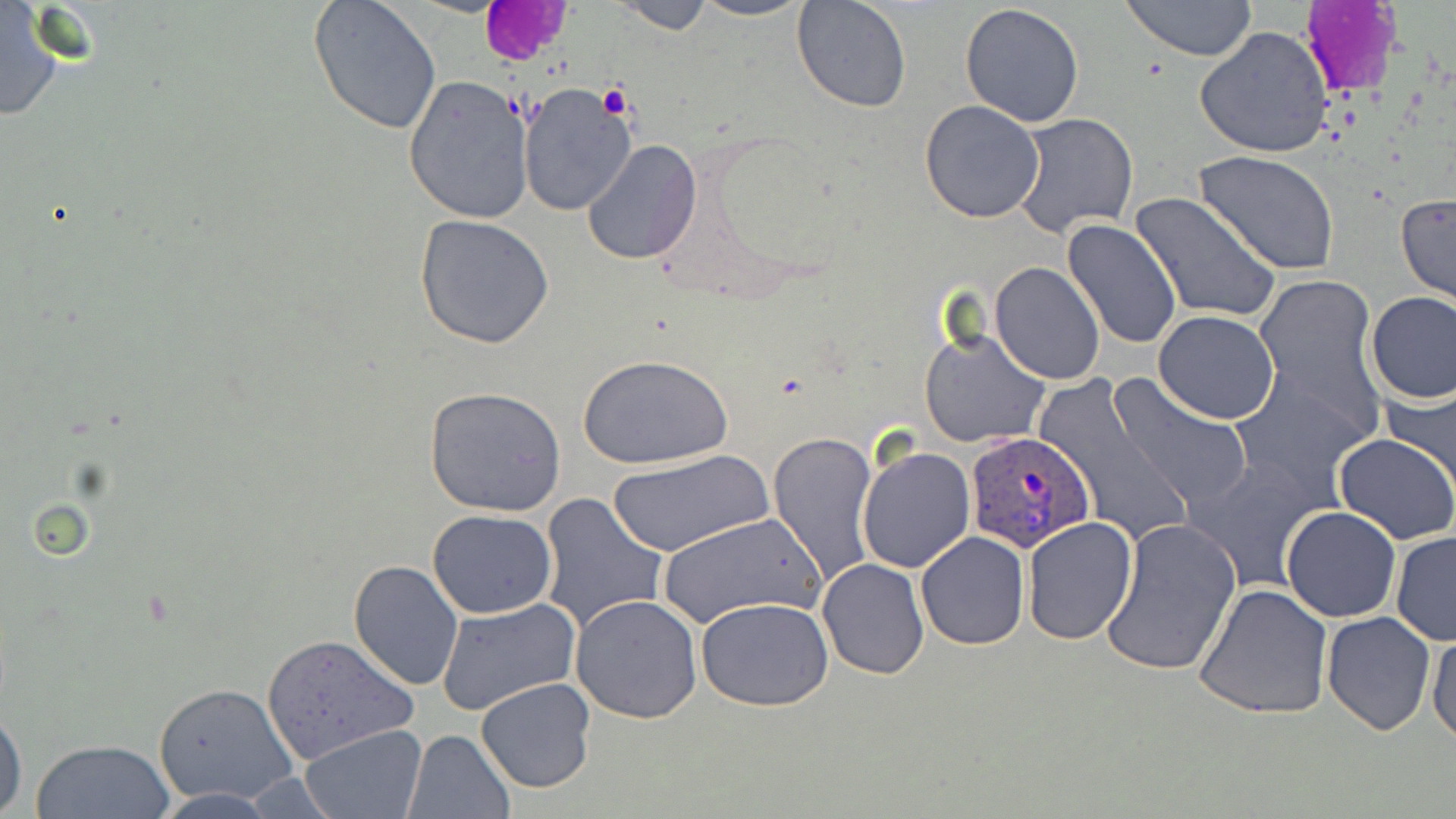
Approximate bounding boxes as (x1, y1, x2, y2) in pixels. Platelet locations: (598, 83, 633, 121). Uninfected red blood cell locations: (686, 0, 815, 22), (792, 0, 911, 112), (1120, 0, 1258, 62), (309, 1, 442, 134), (606, 1, 719, 34), (0, 2, 72, 123), (959, 3, 1084, 127), (1196, 27, 1331, 159), (403, 74, 531, 224), (517, 83, 636, 217), (918, 99, 1046, 223), (1011, 112, 1139, 240), (581, 139, 704, 265), (1194, 150, 1341, 278), (1395, 191, 1455, 310), (1128, 192, 1282, 325), (415, 214, 555, 348), (1061, 220, 1182, 352), (990, 262, 1105, 385), (1250, 276, 1382, 429), (1364, 290, 1456, 405), (1153, 311, 1280, 424), (919, 324, 1049, 450), (578, 353, 733, 469), (1231, 370, 1371, 503), (1030, 374, 1193, 549), (1110, 375, 1253, 512), (1379, 378, 1456, 494), (424, 386, 567, 516), (769, 431, 879, 589), (1333, 432, 1456, 544), (856, 445, 976, 575), (608, 448, 773, 557), (1184, 455, 1328, 594), (538, 492, 669, 632), (1281, 506, 1401, 622), (428, 509, 556, 618), (655, 512, 823, 629), (1021, 517, 1138, 644), (1099, 517, 1242, 678), (1390, 529, 1456, 648), (915, 531, 1030, 650), (349, 558, 464, 689), (817, 558, 930, 679), (1196, 584, 1334, 719), (570, 593, 704, 723), (436, 597, 581, 718), (696, 597, 835, 712), (1322, 610, 1435, 734), (1427, 628, 1456, 745), (261, 632, 416, 765), (477, 676, 597, 793), (153, 682, 303, 806), (0, 702, 27, 817), (299, 724, 427, 818), (403, 729, 514, 818), (28, 737, 176, 819). Plasmodium ovale-infected red blood cell locations: (967, 428, 1097, 553). Slide-level diagnosis: Plasmodium ovale. Single field of view. May-Grünwald-Giemsa stain. Light microscopy. Thin blood smear. Image is 1456×819 pixels. Captured at 1000x magnification.